Locate every blood parasite and identify its species.
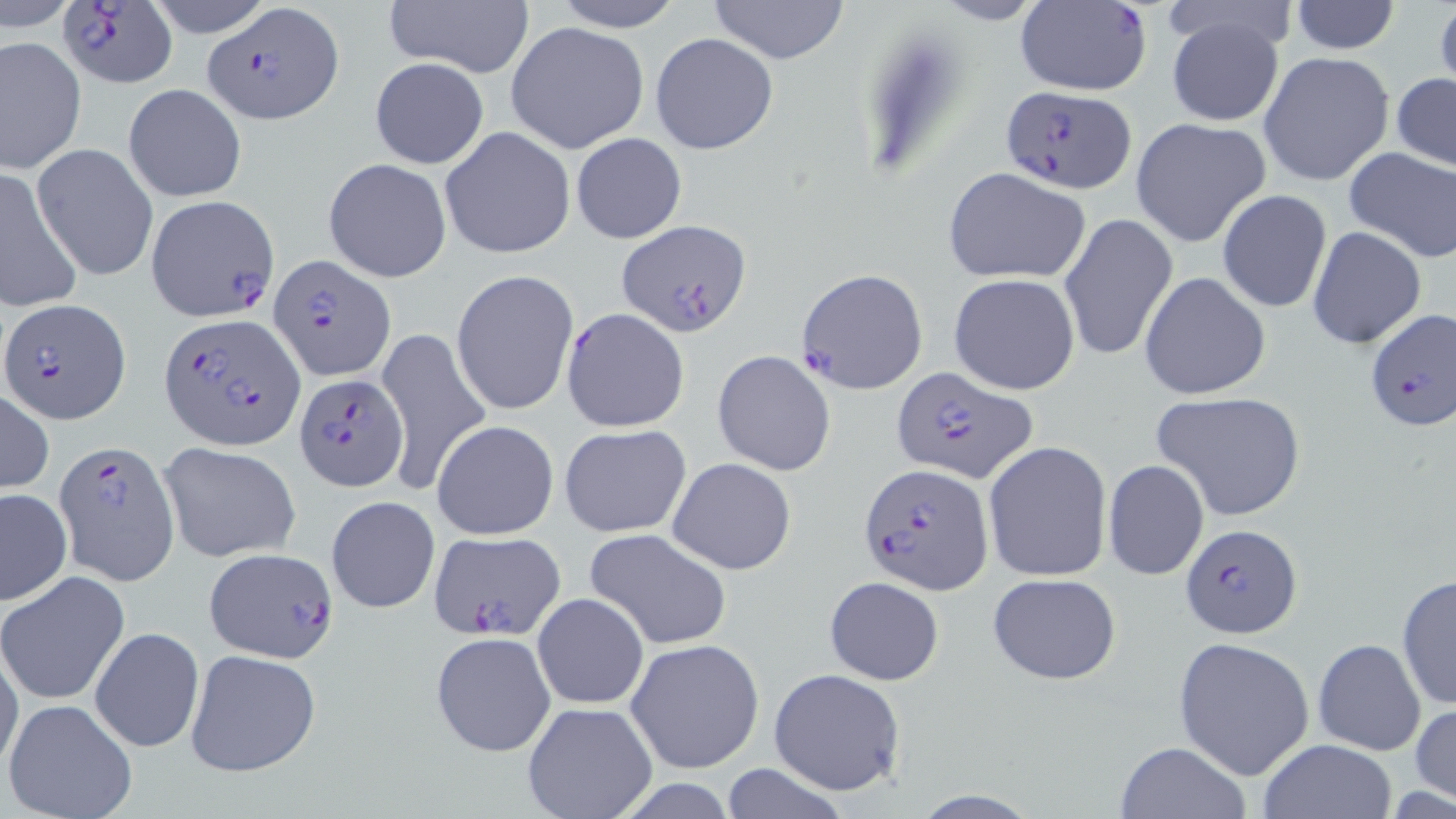

Approximate bounding boxes as (x1, y1, x2, y2) in pixels.
Plasmodium falciparum-infected red blood cells: (56, 0, 177, 90), (204, 2, 341, 123), (1013, 2, 1152, 96), (999, 87, 1136, 194), (145, 193, 281, 319), (616, 220, 749, 338), (271, 256, 396, 380), (798, 269, 928, 392), (1, 297, 127, 424), (1365, 309, 1456, 435), (161, 313, 303, 452), (891, 367, 1037, 484), (296, 375, 405, 492), (56, 440, 179, 587), (861, 464, 992, 594), (1180, 523, 1303, 640), (429, 530, 565, 642), (204, 547, 339, 663).
No Plasmodium ovale, Plasmodium malariae, Plasmodium vivax, Babesia divergens, or Trypanosoma brucei observed.

Uninfected red blood cell locations: (142, 0, 278, 38), (385, 0, 534, 79), (547, 0, 686, 32), (704, 0, 851, 65), (928, 0, 1052, 27), (1291, 1, 1400, 54), (1163, 10, 1287, 127), (505, 21, 649, 155), (650, 33, 778, 156), (2, 35, 87, 174), (1259, 51, 1395, 186), (368, 58, 490, 169), (1392, 72, 1456, 172), (124, 84, 246, 202), (1130, 117, 1275, 249), (439, 126, 576, 261), (570, 132, 686, 243), (33, 143, 159, 282), (1343, 146, 1456, 264), (323, 158, 452, 282), (943, 165, 1092, 282), (0, 166, 85, 312), (1217, 189, 1332, 313), (1061, 214, 1179, 364), (1307, 226, 1427, 350), (450, 268, 580, 418), (1139, 270, 1271, 400), (947, 273, 1081, 394), (562, 308, 690, 431), (374, 322, 494, 498), (711, 350, 836, 477), (0, 389, 53, 495), (1153, 391, 1305, 522), (431, 420, 560, 540), (558, 422, 692, 536), (984, 441, 1113, 583), (158, 443, 300, 563), (668, 457, 796, 575), (1103, 459, 1209, 580), (0, 488, 71, 605), (326, 495, 440, 613), (584, 527, 733, 650), (989, 571, 1121, 685), (0, 572, 129, 705), (1396, 573, 1455, 709), (823, 576, 944, 685), (532, 593, 649, 710), (90, 627, 204, 753), (430, 632, 556, 756), (1173, 636, 1315, 781), (626, 637, 766, 775), (1312, 638, 1426, 755), (0, 641, 23, 783), (185, 648, 323, 777), (769, 668, 906, 795), (3, 699, 138, 819), (521, 701, 657, 819), (1411, 701, 1455, 807), (1258, 740, 1397, 819), (1116, 742, 1252, 819), (718, 761, 854, 819). Slide-level diagnosis: Plasmodium falciparum. Single field of view. Light microscopy. Thin blood film. Image is 1456×819 pixels. Captured at 1000x magnification. May-Grünwald-Giemsa stain.